Identify the parasite.
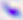

This is Toxoplasma gondii.

{
  "modality": "photomicrograph",
  "magnification": "400x"
}